Identify the preparation type.
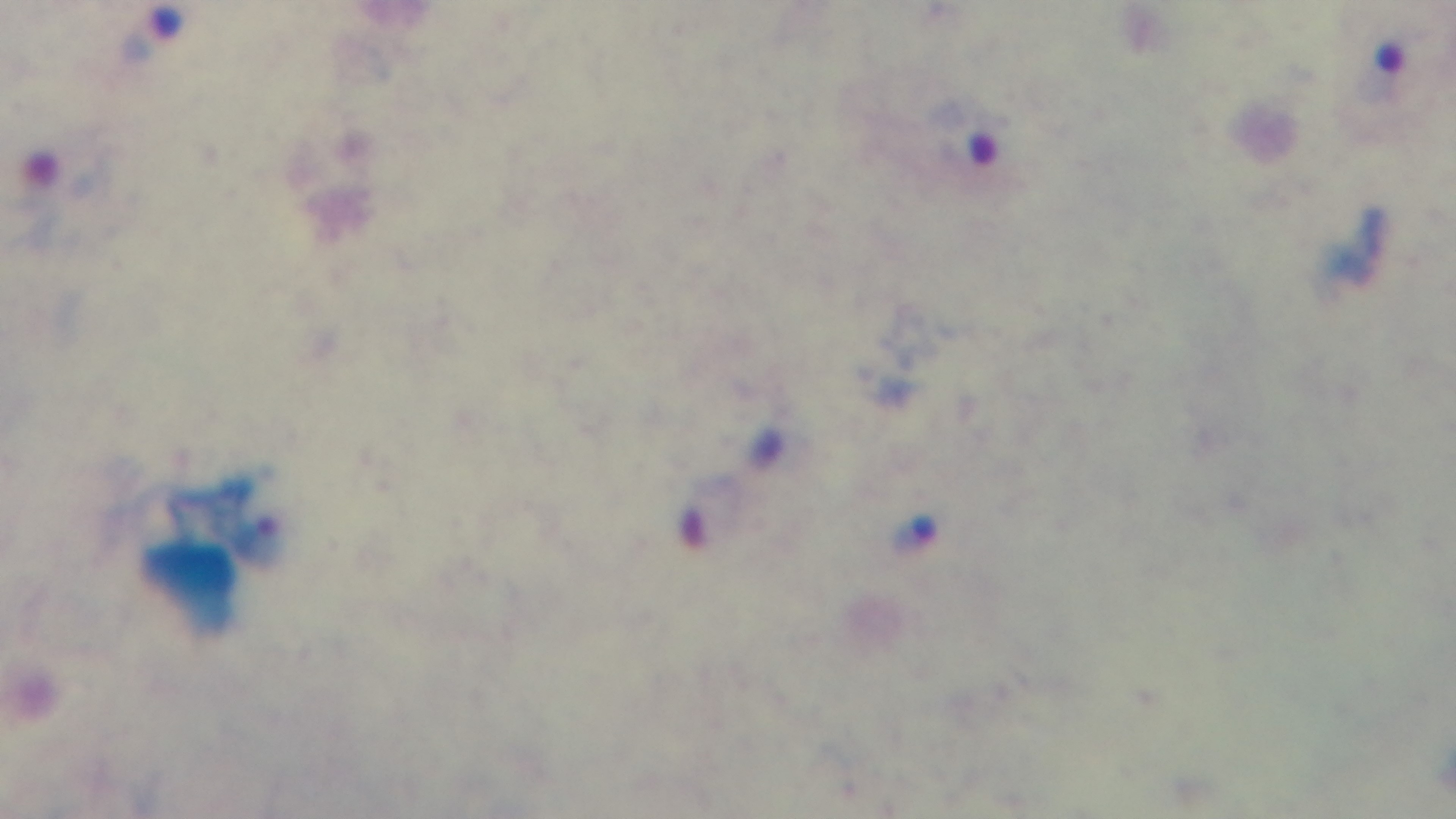
A thick smear.

One field from the slide. Mounted 4K digital camera. Malaria status: infected. Light microscopy. 100x oil-immersion objective. Giemsa stain.